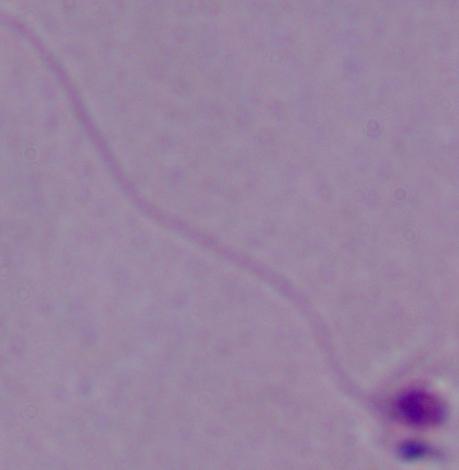
modality: photomicrograph
magnification: 1000x
identification: Leishmania